Report the malaria status of this cell.
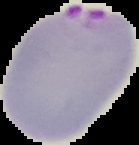

It is parasitized.

Summary:
  - Image type: cell region segmented out of the field of view; surrounding area masked to black
  - Preparation: thin blood film
  - Image size: 139×145 pixels